Report the malaria status of this cell.
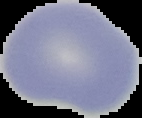
It is uninfected.

preparation = thin blood smear
image size = 142×118 pixels
image type = segmented cell region on a black background